Assess this cell for malaria.
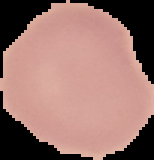

It is uninfected.

preparation: thin blood film
image_type: segmented cell region on a black background
image_size: 154×160 pixels